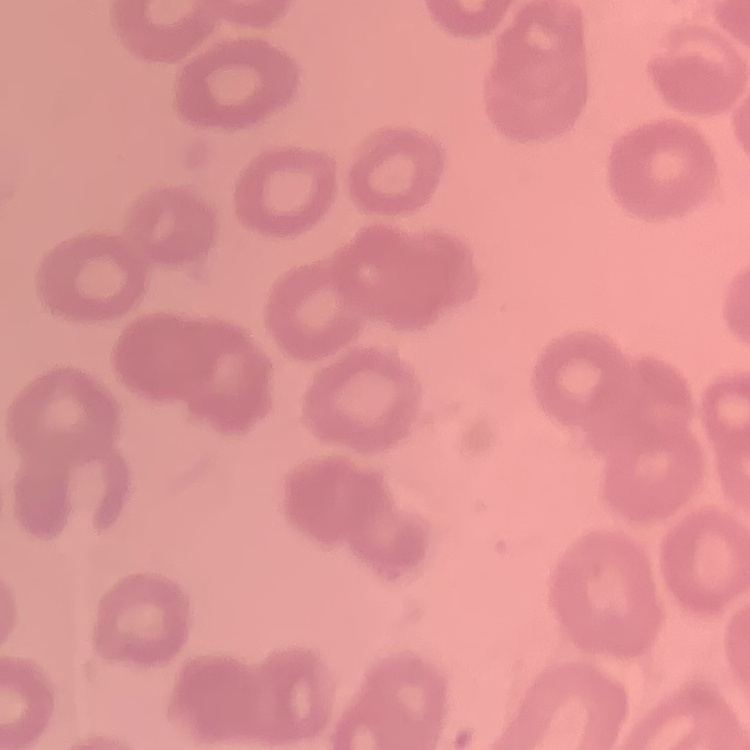
erythrocyte morphology = no rouleaux formation
image type = square crop of a larger photomicrograph
preparation = thin peripheral smear
stain = Field's or Giemsa